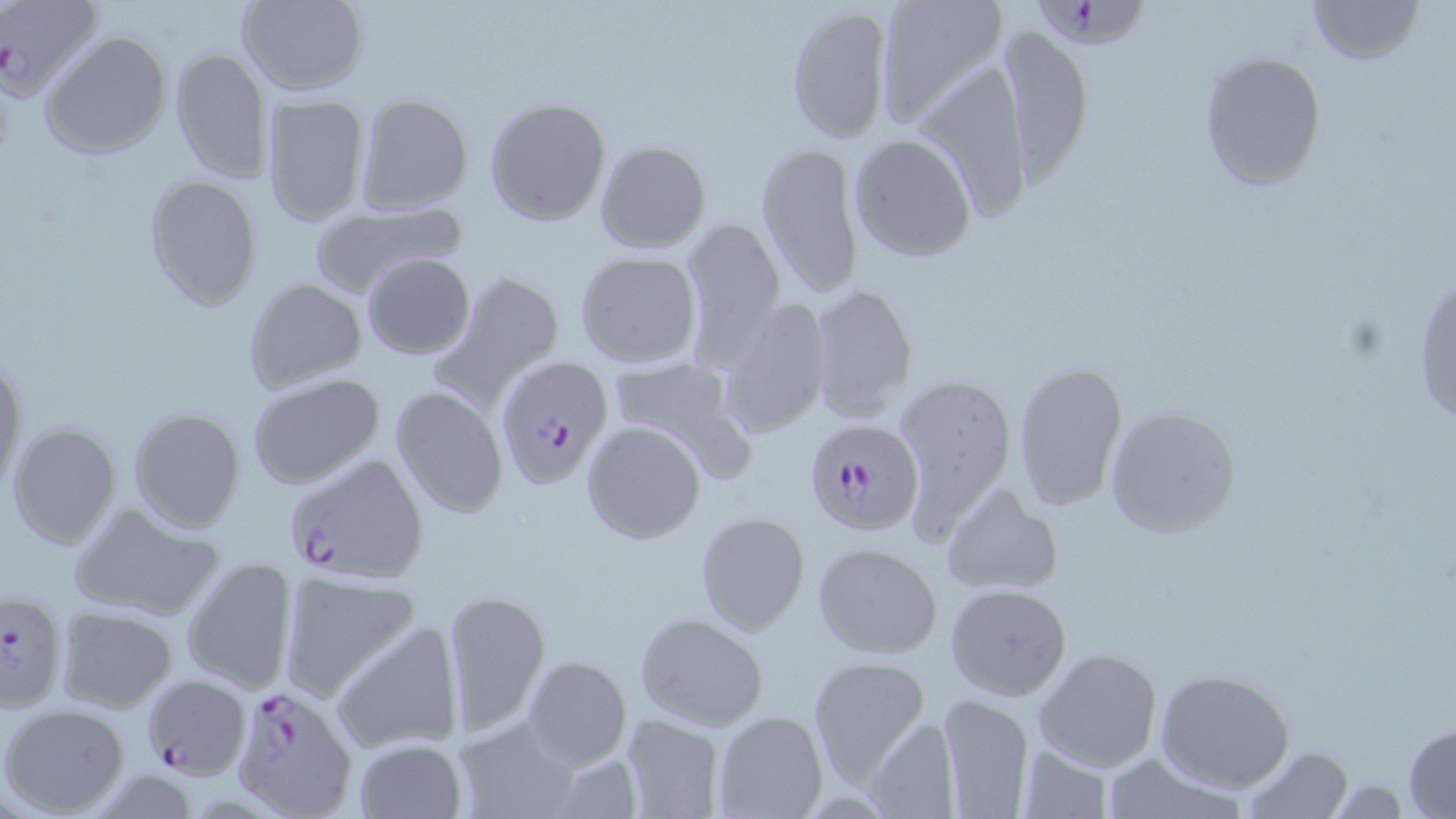

Approximate bounding boxes as [x1, y1, x2, y2] in pixels. Plasmodium falciparum-infected red blood cell locations: [2, 0, 103, 102], [1030, 4, 1150, 55], [497, 356, 614, 488], [802, 416, 925, 535], [282, 451, 427, 584], [1, 590, 69, 715], [140, 674, 251, 780], [229, 680, 359, 817]. Uninfected red blood cell locations: [234, 0, 370, 95], [872, 0, 1009, 130], [1308, 0, 1424, 67], [784, 5, 895, 144], [995, 25, 1094, 185], [40, 30, 172, 160], [169, 46, 272, 183], [1196, 50, 1328, 192], [912, 63, 1034, 225], [355, 93, 475, 215], [260, 94, 372, 227], [484, 96, 611, 227], [848, 132, 976, 262], [593, 140, 712, 254], [755, 141, 865, 299], [142, 174, 262, 310], [309, 200, 467, 297], [679, 217, 786, 365], [573, 251, 703, 369], [361, 253, 475, 360], [1412, 264, 1455, 431], [433, 268, 565, 409], [242, 277, 368, 395], [808, 281, 918, 423], [714, 298, 832, 439], [0, 348, 27, 498], [605, 355, 749, 473], [1011, 358, 1128, 516], [245, 371, 386, 492], [892, 372, 1018, 534], [390, 385, 509, 518], [1104, 404, 1243, 537], [128, 406, 246, 533], [580, 419, 708, 545], [6, 421, 123, 549], [942, 482, 1062, 597], [68, 499, 227, 621], [695, 510, 811, 637], [812, 541, 945, 660], [181, 556, 297, 695], [277, 572, 421, 701], [944, 582, 1071, 702], [441, 588, 551, 737], [56, 606, 179, 713], [633, 611, 769, 731], [331, 618, 464, 755], [1033, 646, 1165, 774], [521, 654, 632, 769], [805, 654, 930, 789], [1153, 669, 1297, 793], [938, 692, 1035, 817], [1, 704, 131, 817], [713, 711, 828, 819], [864, 713, 962, 818], [619, 714, 724, 819], [453, 715, 583, 819], [1402, 724, 1456, 817], [351, 736, 469, 819], [1015, 743, 1117, 819], [1241, 744, 1355, 817], [1098, 751, 1249, 819]. Slide-level diagnosis: Plasmodium falciparum. Captured at 1000x magnification. Single field of view. Image is 1456×819 pixels. Thin blood film. Optical microscopy. May-Grünwald-Giemsa-stained preparation.